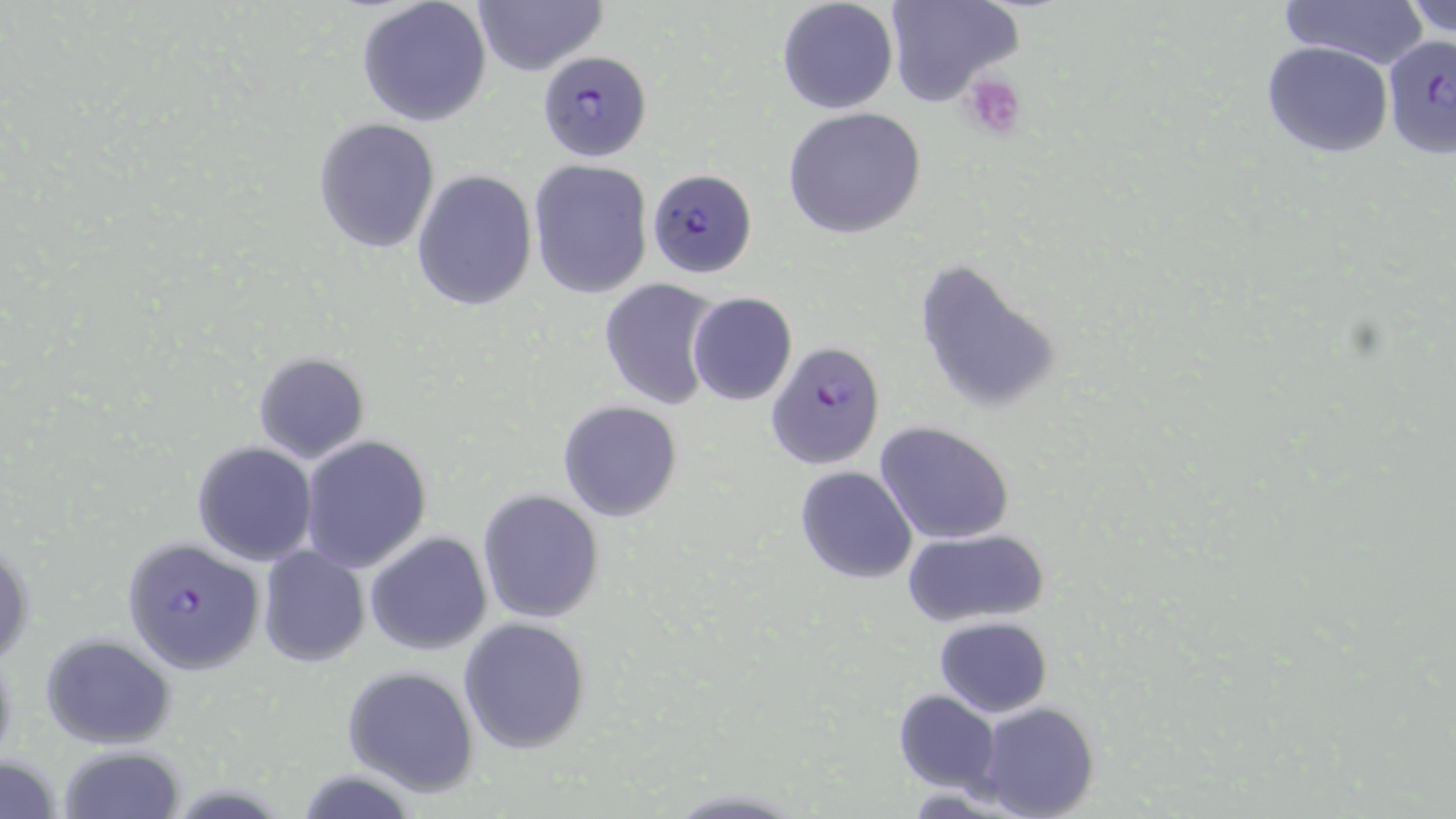

Approximate bounding boxes as named x1/y1/x2/y2 corners in pixels. Platelet locations: (x1=961, y1=73, x2=1026, y2=140). Plasmodium falciparum-infected red blood cell locations: (x1=1382, y1=34, x2=1455, y2=159), (x1=537, y1=52, x2=651, y2=159), (x1=646, y1=168, x2=754, y2=277), (x1=766, y1=341, x2=886, y2=470), (x1=120, y1=536, x2=265, y2=674). Uninfected red blood cell locations: (x1=356, y1=0, x2=492, y2=126), (x1=470, y1=0, x2=606, y2=77), (x1=887, y1=0, x2=1023, y2=109), (x1=1277, y1=0, x2=1428, y2=69), (x1=1402, y1=0, x2=1456, y2=39), (x1=775, y1=1, x2=899, y2=115), (x1=1263, y1=41, x2=1394, y2=159), (x1=782, y1=107, x2=927, y2=239), (x1=313, y1=118, x2=439, y2=253), (x1=528, y1=160, x2=654, y2=300), (x1=412, y1=169, x2=539, y2=311), (x1=912, y1=255, x2=1063, y2=416), (x1=598, y1=280, x2=718, y2=411), (x1=686, y1=292, x2=797, y2=407), (x1=253, y1=353, x2=370, y2=463), (x1=557, y1=400, x2=683, y2=522), (x1=875, y1=421, x2=1017, y2=546), (x1=299, y1=435, x2=433, y2=573), (x1=192, y1=442, x2=317, y2=566), (x1=795, y1=466, x2=917, y2=584), (x1=477, y1=489, x2=604, y2=624), (x1=901, y1=527, x2=1048, y2=628), (x1=365, y1=532, x2=492, y2=656), (x1=1, y1=536, x2=33, y2=670), (x1=257, y1=547, x2=369, y2=667), (x1=935, y1=615, x2=1053, y2=718), (x1=458, y1=617, x2=592, y2=753), (x1=41, y1=634, x2=175, y2=749), (x1=343, y1=665, x2=480, y2=795), (x1=892, y1=690, x2=1000, y2=794), (x1=974, y1=703, x2=1102, y2=819), (x1=60, y1=744, x2=185, y2=819), (x1=0, y1=749, x2=66, y2=819), (x1=666, y1=787, x2=803, y2=816). Slide-level diagnosis: Plasmodium falciparum. Light microscopy. One field of a larger specimen. Image is 1456×819 pixels. Thin blood smear. 1000x magnification. May-Grünwald-Giemsa stain.